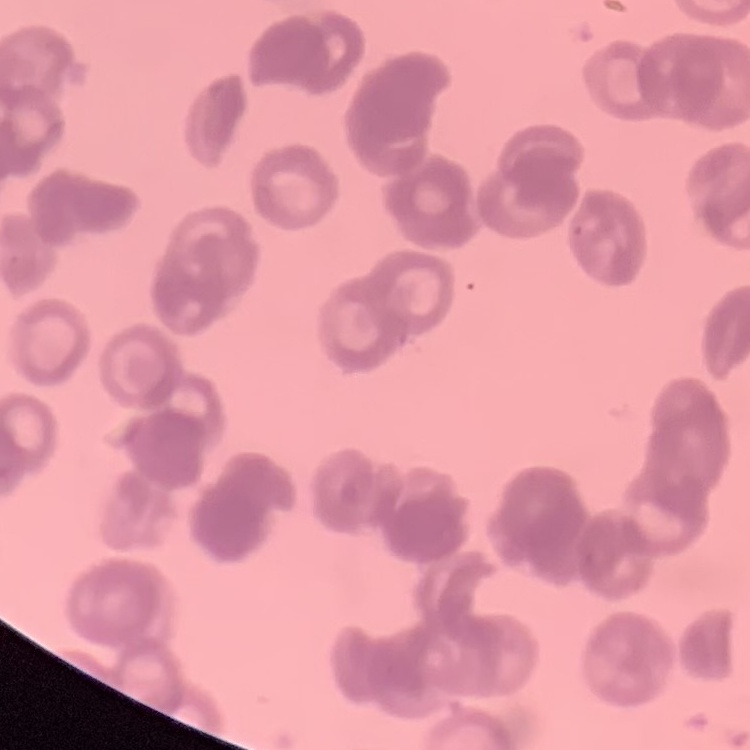

The red blood cells show rouleaux formation. One tile cut from a larger photomicrograph. Thin blood smear. Stained with either Field's or Giemsa.